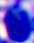

A white blood cell is shown. Captured at 400x magnification. Micrograph.